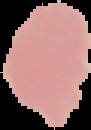

Result: no Plasmodium parasites detected. Image is 91×130 pixels. From a thin blood smear. Cell region segmented out of the field of view; the surrounding area is masked to black.